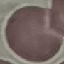

malaria status = uninfected
preparation = thin blood film
image type = automatically extracted cell patch, resized to 64 × 64 pixels
stain = Giemsa
capture = smartphone through the microscope eyepiece